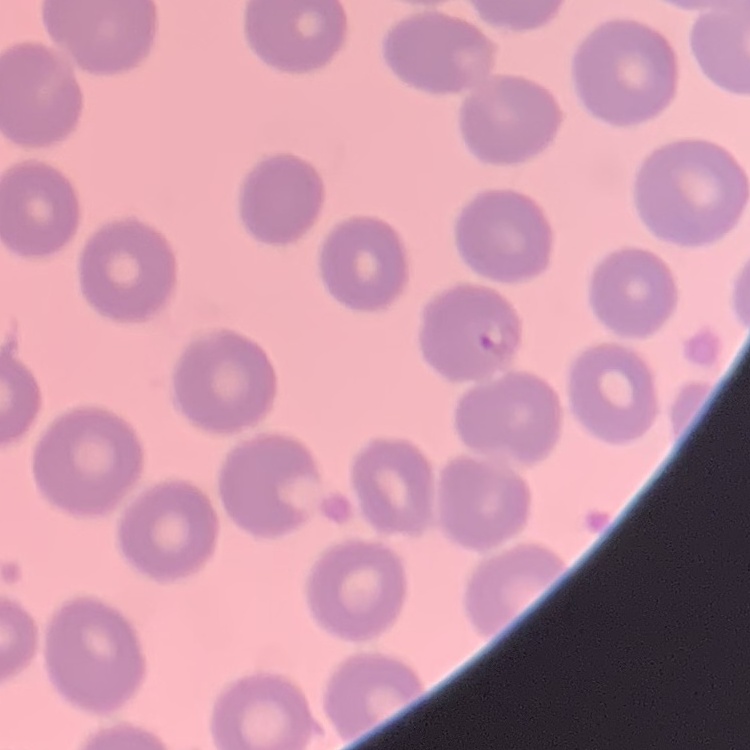

erythrocyte_morphology: no rouleaux formation
stain: Field's or Giemsa
preparation: thin peripheral smear
image_type: one tile cut from a larger photomicrograph